Give the preparation type.
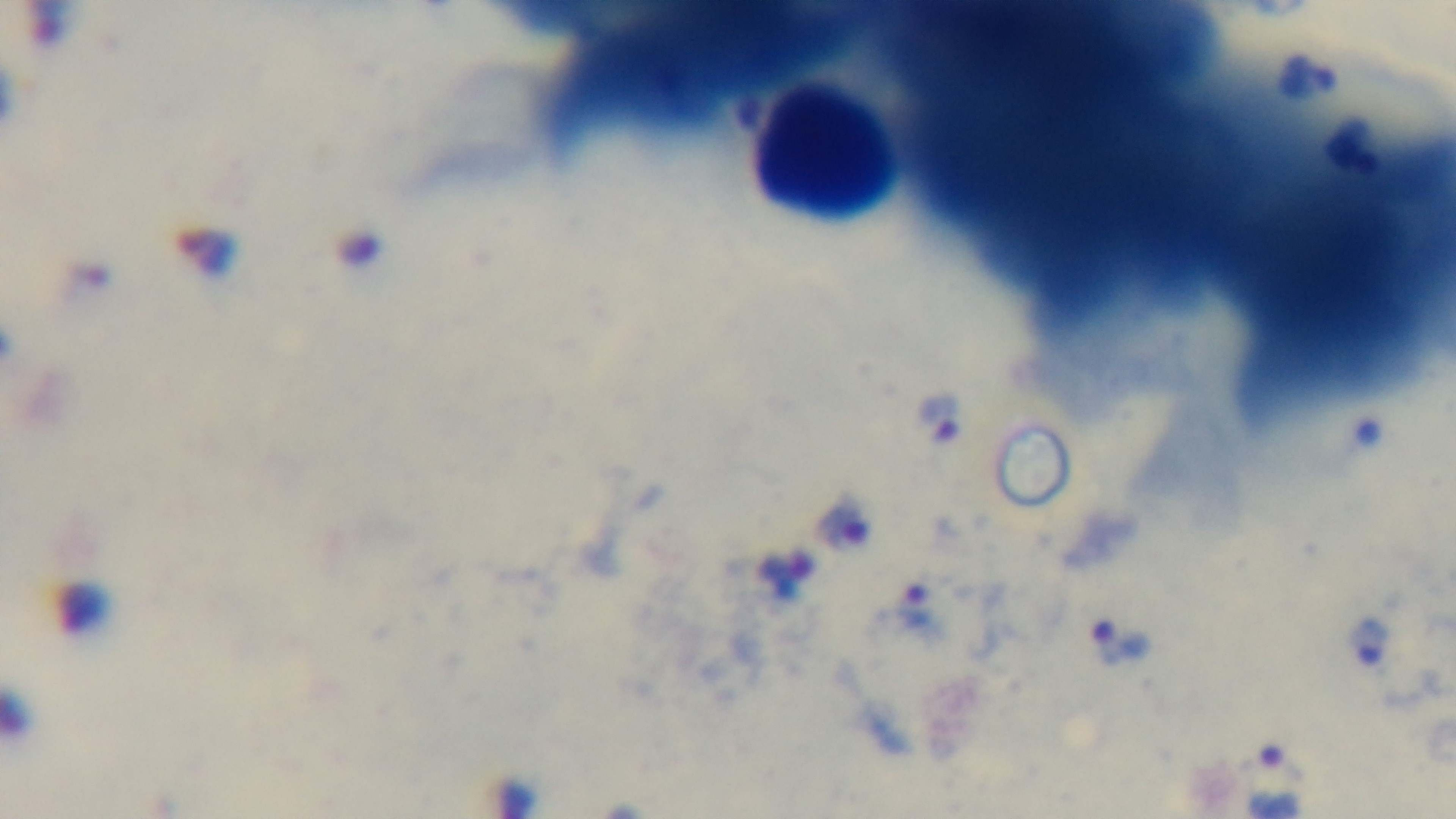
Thick.

{
  "objective": "100x oil immersion",
  "field_of_view": "single",
  "stain": "Giemsa",
  "modality": "light microscopy",
  "malaria_status": "positive",
  "capture": "mounted 4K digital camera"
}